State which parasite is depicted.
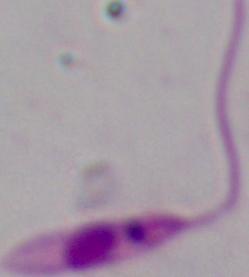
Leishmania.

{
  "magnification": "1000x",
  "modality": "photomicrograph"
}